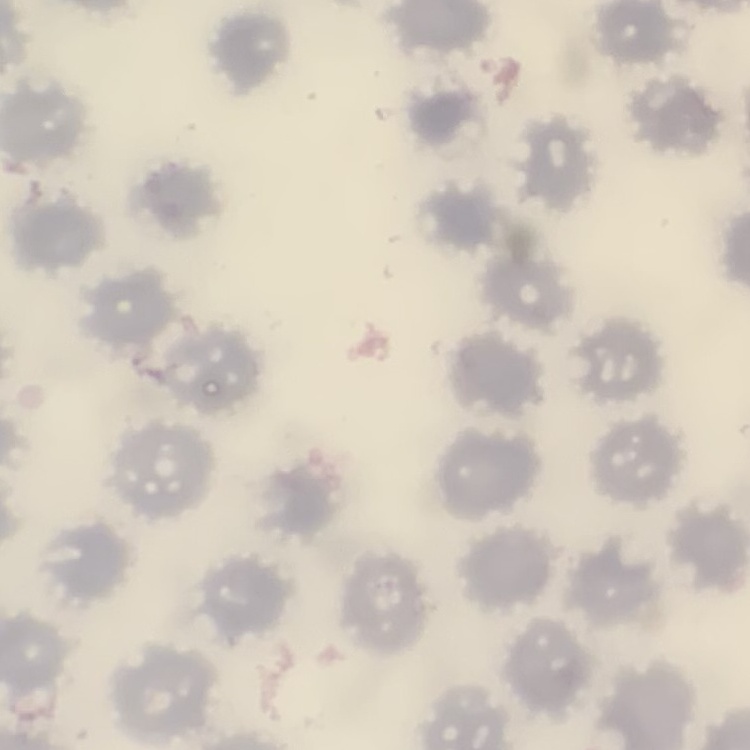

Summary:
  - Erythrocyte morphology: no rouleaux formation
  - Image type: one tile cut from a larger photomicrograph
  - Stain: Field's or Giemsa
  - Preparation: thin blood smear